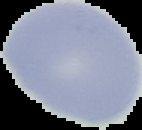
Summary:
  - Preparation: thin blood smear
  - Image type: cell region segmented out of the field of view; surrounding area masked to black
  - Malaria status: uninfected
  - Image size: 142×130 pixels